Describe the morphology of the erythrocytes.
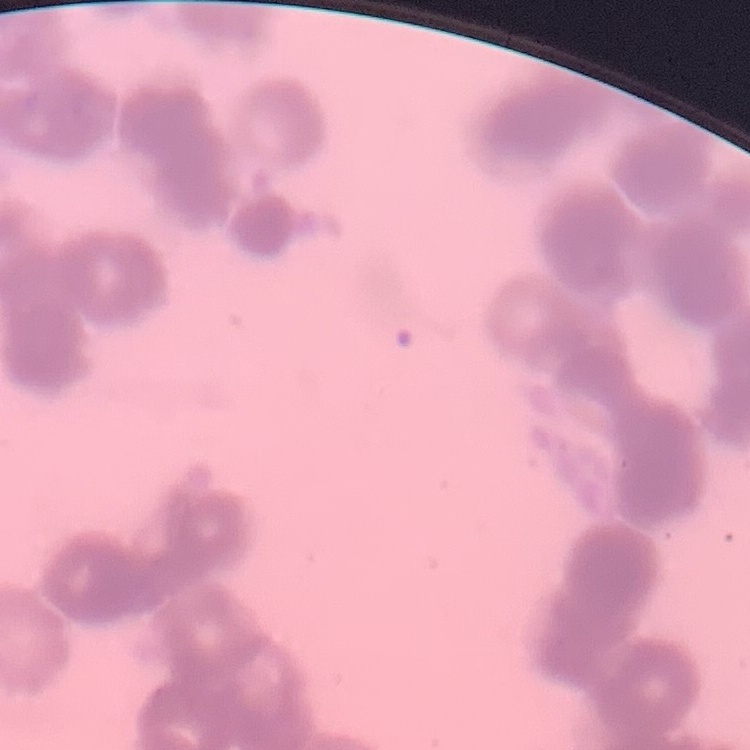

Rouleaux formation.

Summary:
  - Stain: Field's or Giemsa
  - Preparation: thin blood smear
  - Image type: one tile cut from a larger photomicrograph